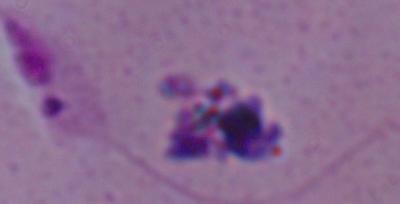
identification = Leishmania
modality = photomicrograph
magnification = 1000x